State which parasite is depicted.
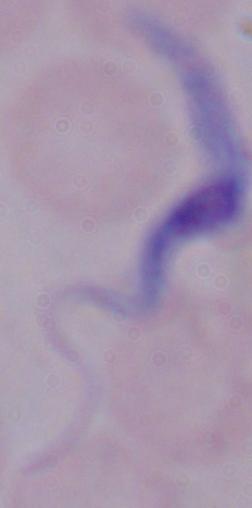

This is a trypanosome.

Micrograph. 1000x magnification.